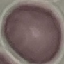

Summary:
  - Result: no malaria parasites seen
  - Stain: Giemsa
  - Image type: automatically extracted cell patch, resized to 64 × 64 pixels
  - Capture: smartphone camera at the microscope eyepiece
  - Preparation: thin blood smear